State which cell type is depicted.
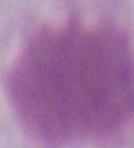

This is an erythrocyte.

Summary:
  - Modality: micrograph
  - Magnification: 1000x